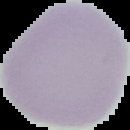

preparation: thin blood film
image_size: 130×130 pixels
result: negative for malaria parasites
image_type: segmented cell region with the area outside set to black